Report the malaria status of this cell.
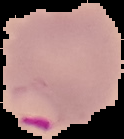
Parasitized.

Summary:
  - Preparation: thin blood smear
  - Image type: segmented cell region with the area outside set to black
  - Image size: 124×139 pixels